State which parasite is depicted.
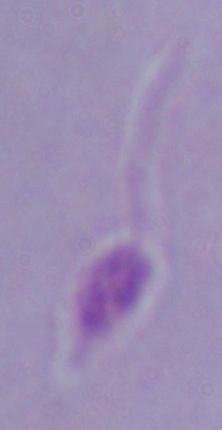

Leishmania.

Micrograph. Captured at 1000x magnification.